Locate and identify every blood parasite.
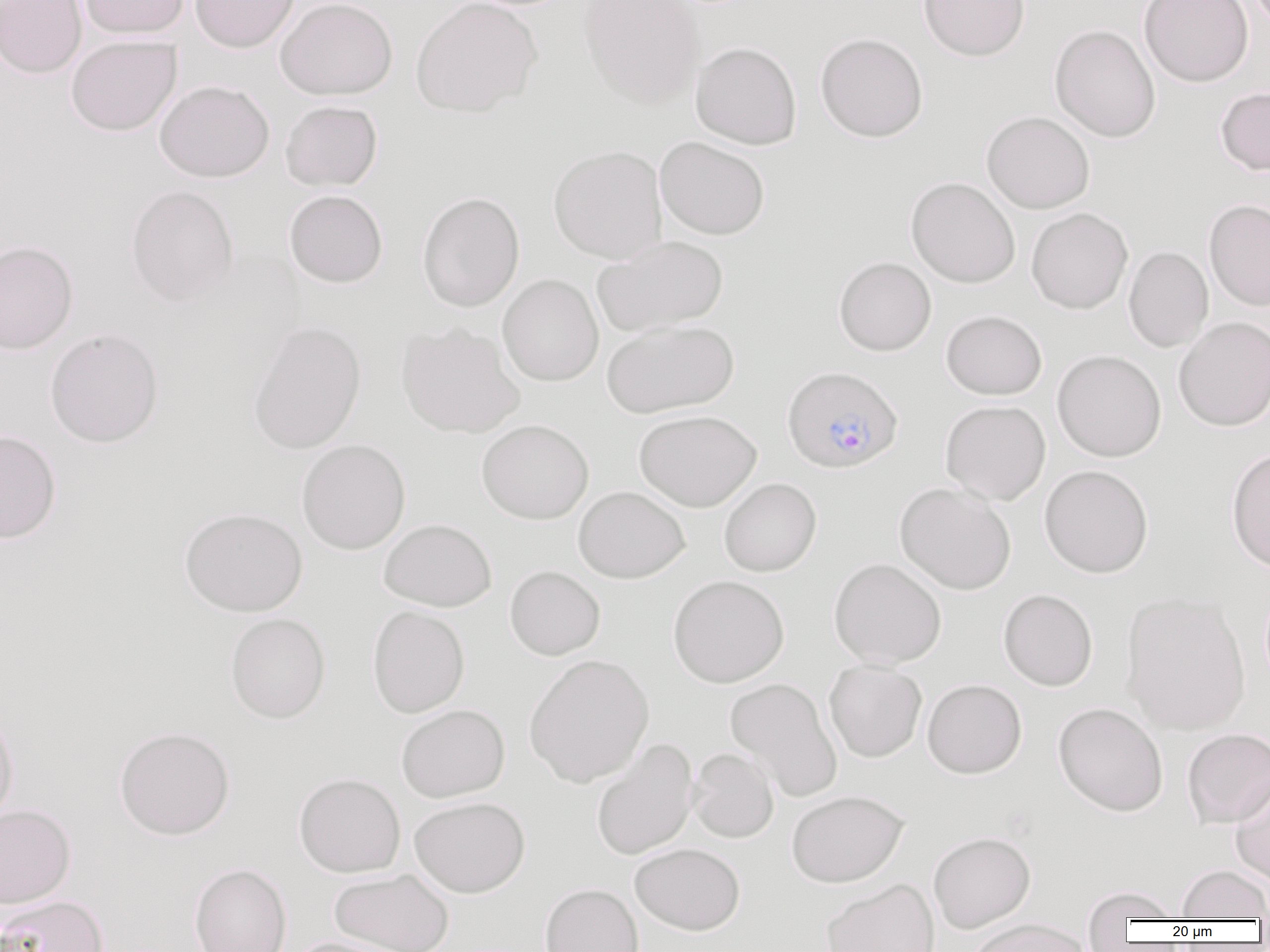

Approximate bounding boxes as named x1/y1/x2/y2 corners in pixels.
Plasmodium falciparum-infected red blood cells: (x1=782, y1=365, x2=903, y2=474).
No Plasmodium ovale, Plasmodium malariae, Plasmodium vivax, Babesia divergens, or Trypanosoma brucei observed.

slide-level diagnosis = Plasmodium falciparum
field of view = one of a larger specimen
uninfected red blood cell locations = approximate bounding boxes as named x1/y1/x2/y2 corners in pixels: (x1=0, y1=0, x2=87, y2=78), (x1=78, y1=0, x2=190, y2=39), (x1=190, y1=0, x2=299, y2=53), (x1=275, y1=0, x2=398, y2=100), (x1=410, y1=0, x2=542, y2=117), (x1=578, y1=0, x2=705, y2=109), (x1=918, y1=0, x2=1031, y2=61), (x1=1138, y1=0, x2=1254, y2=88), (x1=1049, y1=24, x2=1161, y2=143), (x1=815, y1=32, x2=928, y2=142), (x1=66, y1=35, x2=182, y2=136), (x1=690, y1=41, x2=802, y2=149), (x1=155, y1=80, x2=274, y2=183), (x1=1216, y1=86, x2=1270, y2=176), (x1=280, y1=100, x2=382, y2=191), (x1=981, y1=111, x2=1095, y2=214), (x1=655, y1=136, x2=770, y2=240), (x1=548, y1=145, x2=667, y2=264), (x1=906, y1=176, x2=1021, y2=288), (x1=125, y1=185, x2=239, y2=306), (x1=284, y1=189, x2=388, y2=288), (x1=417, y1=191, x2=525, y2=312), (x1=1203, y1=199, x2=1270, y2=311), (x1=1026, y1=208, x2=1133, y2=314), (x1=592, y1=235, x2=729, y2=336), (x1=0, y1=240, x2=78, y2=354), (x1=1123, y1=246, x2=1214, y2=352), (x1=834, y1=256, x2=936, y2=356), (x1=498, y1=274, x2=604, y2=386), (x1=940, y1=309, x2=1047, y2=399), (x1=1173, y1=316, x2=1270, y2=432), (x1=601, y1=319, x2=740, y2=418), (x1=247, y1=321, x2=367, y2=454), (x1=396, y1=322, x2=524, y2=438), (x1=44, y1=328, x2=164, y2=448), (x1=1052, y1=349, x2=1166, y2=462), (x1=940, y1=400, x2=1051, y2=505), (x1=634, y1=409, x2=762, y2=511), (x1=477, y1=419, x2=594, y2=524), (x1=0, y1=429, x2=62, y2=544), (x1=296, y1=439, x2=411, y2=555), (x1=1226, y1=447, x2=1270, y2=573), (x1=1039, y1=464, x2=1154, y2=578), (x1=719, y1=477, x2=821, y2=576), (x1=895, y1=482, x2=1016, y2=595), (x1=573, y1=486, x2=690, y2=583), (x1=179, y1=507, x2=307, y2=616), (x1=379, y1=518, x2=497, y2=611), (x1=829, y1=558, x2=946, y2=669), (x1=504, y1=565, x2=605, y2=660), (x1=668, y1=574, x2=789, y2=688), (x1=998, y1=588, x2=1098, y2=691), (x1=1120, y1=591, x2=1251, y2=735), (x1=368, y1=605, x2=470, y2=718), (x1=225, y1=613, x2=330, y2=723), (x1=524, y1=653, x2=655, y2=787), (x1=824, y1=659, x2=927, y2=762), (x1=724, y1=676, x2=843, y2=803), (x1=922, y1=678, x2=1027, y2=779), (x1=1053, y1=702, x2=1168, y2=816), (x1=396, y1=704, x2=510, y2=803), (x1=0, y1=712, x2=19, y2=826), (x1=114, y1=726, x2=235, y2=840), (x1=1182, y1=728, x2=1270, y2=828), (x1=591, y1=738, x2=699, y2=860), (x1=687, y1=747, x2=779, y2=843), (x1=294, y1=772, x2=406, y2=877), (x1=1229, y1=772, x2=1270, y2=884), (x1=786, y1=790, x2=908, y2=887), (x1=409, y1=796, x2=530, y2=898), (x1=0, y1=804, x2=76, y2=908), (x1=928, y1=831, x2=1036, y2=933), (x1=630, y1=842, x2=745, y2=936), (x1=189, y1=863, x2=292, y2=952), (x1=1176, y1=865, x2=1270, y2=920), (x1=329, y1=869, x2=455, y2=952), (x1=821, y1=878, x2=940, y2=952), (x1=540, y1=882, x2=643, y2=952), (x1=1080, y1=885, x2=1183, y2=932), (x1=0, y1=895, x2=109, y2=952), (x1=966, y1=918, x2=1092, y2=952), (x1=283, y1=936, x2=410, y2=952)
preparation = thin blood film
modality = optical microscopy
magnification = 1000x
image size = 1270×952 pixels